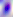
Toxoplasma gondii is seen. Photomicrograph. Captured at 400x magnification.